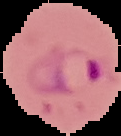
Image is 121×136 pixels. From a thin blood smear. Malaria status: parasitized. Cell region segmented out of the field of view; the surrounding area is masked to black.